Comment on the morphology of the erythrocytes.
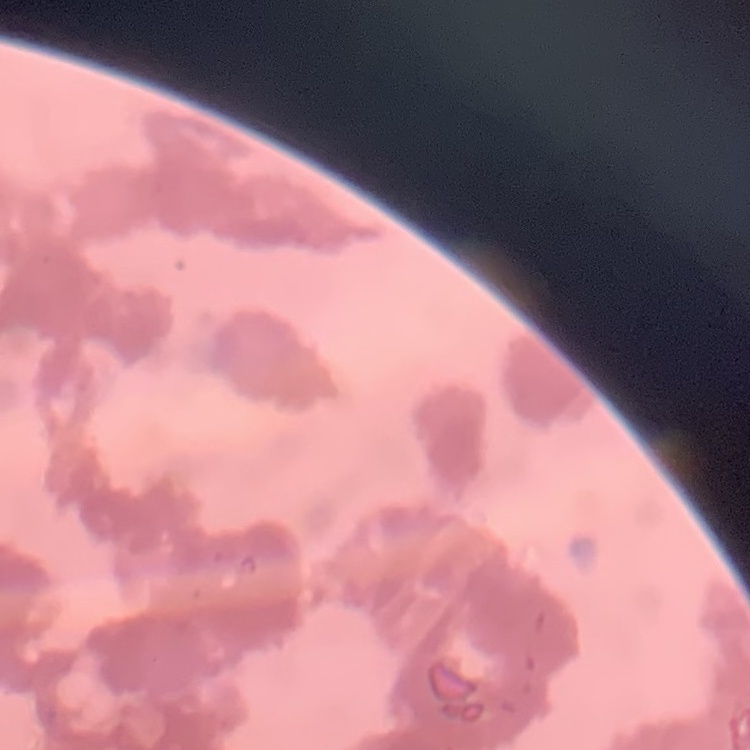

They show rouleaux formation.

preparation = thin peripheral smear
stain = Field's or Giemsa
image type = square crop of a larger photomicrograph